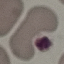

malaria status = uninfected
image type = cell patch, automatically extracted from a larger field of view and resized to 64 × 64 pixels
preparation = thin blood smear
stain = Giemsa
capture = smartphone through the microscope eyepiece